Point out every malaria parasite and every leukocyte.
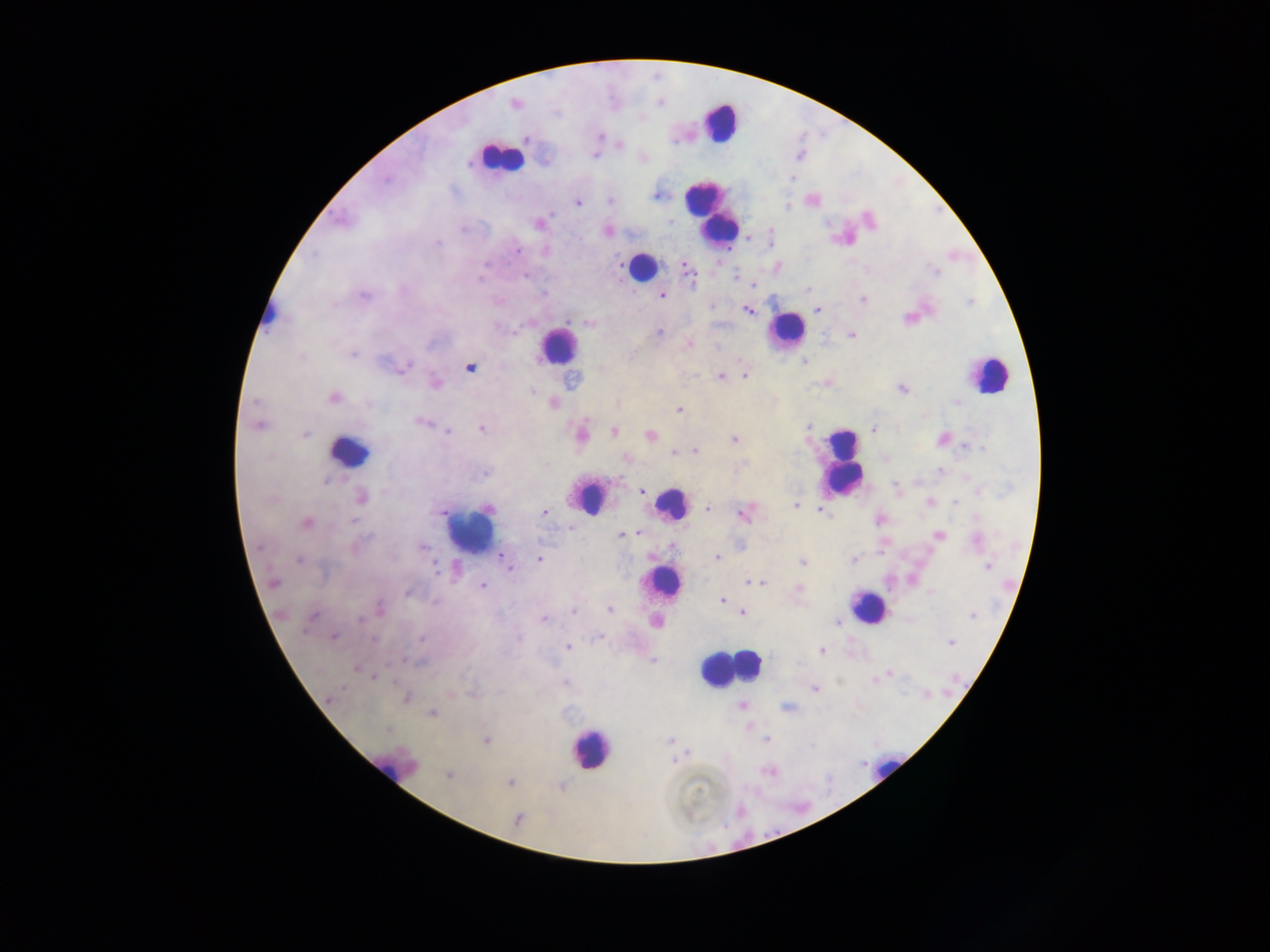

Approximate centers as [x, y] in pixels.
Malaria parasites: [515, 103], [600, 136], [527, 138], [619, 145], [594, 156], [468, 162], [792, 177], [386, 179], [655, 195], [610, 200], [577, 203], [787, 206], [538, 224], [461, 229], [607, 231], [437, 243], [517, 251], [314, 255], [688, 271], [936, 272], [526, 275], [735, 275], [479, 279], [754, 285], [807, 289], [544, 294], [364, 295], [661, 295], [864, 300], [334, 304], [711, 306], [818, 309], [747, 311], [588, 324], [514, 331], [658, 332], [852, 335], [688, 345], [353, 354], [301, 356], [805, 362], [406, 366], [470, 368], [600, 369], [744, 375], [720, 376], [436, 383], [903, 389], [531, 391], [335, 399], [255, 402], [956, 402], [554, 403], [369, 404], [616, 404], [679, 410], [420, 422], [258, 426], [481, 428], [808, 428], [873, 430], [447, 432], [614, 432], [304, 434], [582, 434], [650, 435], [941, 438], [734, 440], [964, 446], [981, 448], [696, 451], [673, 452], [626, 458], [939, 470], [487, 474], [325, 481], [641, 491], [979, 491], [362, 497], [930, 502], [954, 503], [796, 506], [708, 508], [488, 509], [823, 511], [544, 513], [744, 513], [353, 521], [306, 523], [636, 533], [621, 535], [939, 535], [976, 540], [422, 547], [502, 557], [717, 557], [539, 560], [853, 560], [299, 561], [803, 562], [987, 566], [510, 568], [435, 569], [273, 582], [755, 583], [761, 583], [482, 586], [799, 589], [407, 593], [930, 593], [723, 600], [380, 609], [610, 610], [574, 612], [742, 612], [973, 616], [311, 618], [359, 619], [543, 619], [837, 622], [334, 637], [600, 637], [374, 639], [421, 639], [951, 642], [568, 647], [822, 650], [653, 660], [356, 669], [890, 674], [374, 677], [565, 682], [342, 688], [814, 689], [927, 694], [330, 698], [407, 698], [741, 706], [787, 708], [432, 713], [388, 729], [766, 739], [486, 740], [670, 741], [674, 760], [768, 771], [448, 775], [510, 783], [518, 818].
Leukocytes: [720, 123], [500, 157], [710, 211], [642, 266], [270, 318], [785, 331], [557, 346], [988, 374], [350, 452], [842, 462], [589, 497], [671, 503], [470, 531], [666, 582], [867, 606], [728, 669], [589, 748], [393, 770], [882, 770].

country = Ghana
image size = 1270×952 pixels
field of view = single
capture = mobile-phone photograph through a microscope
preparation = thick blood film